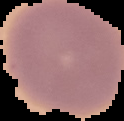
Cell region segmented out of the field of view; the surrounding area is masked to black. Result: no malaria parasites seen. From a thin blood smear. Image is 124×121 pixels.